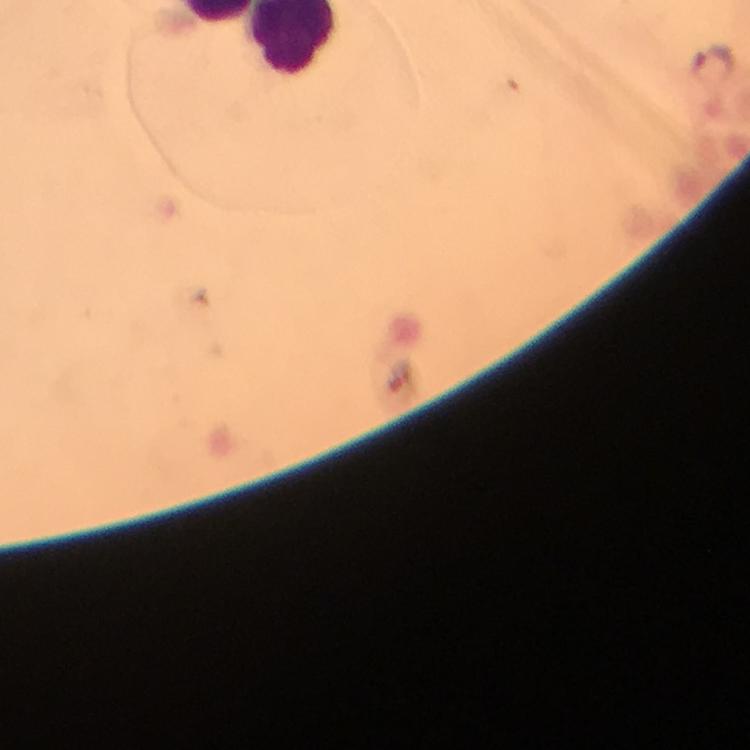
Approximate centers as {x, y} in pixels. Malaria parasite locations: {717, 68}. Image is 750×750 pixels. From a malaria diagnostic workup. At 100x magnification. Immersion oil applied. Cropped region of a single field of view. Giemsa-stained preparation. Photographed with a smartphone mounted on the microscope. Thick smear.